Give the extent of all Plasmodium ovale-infected red blood cells.
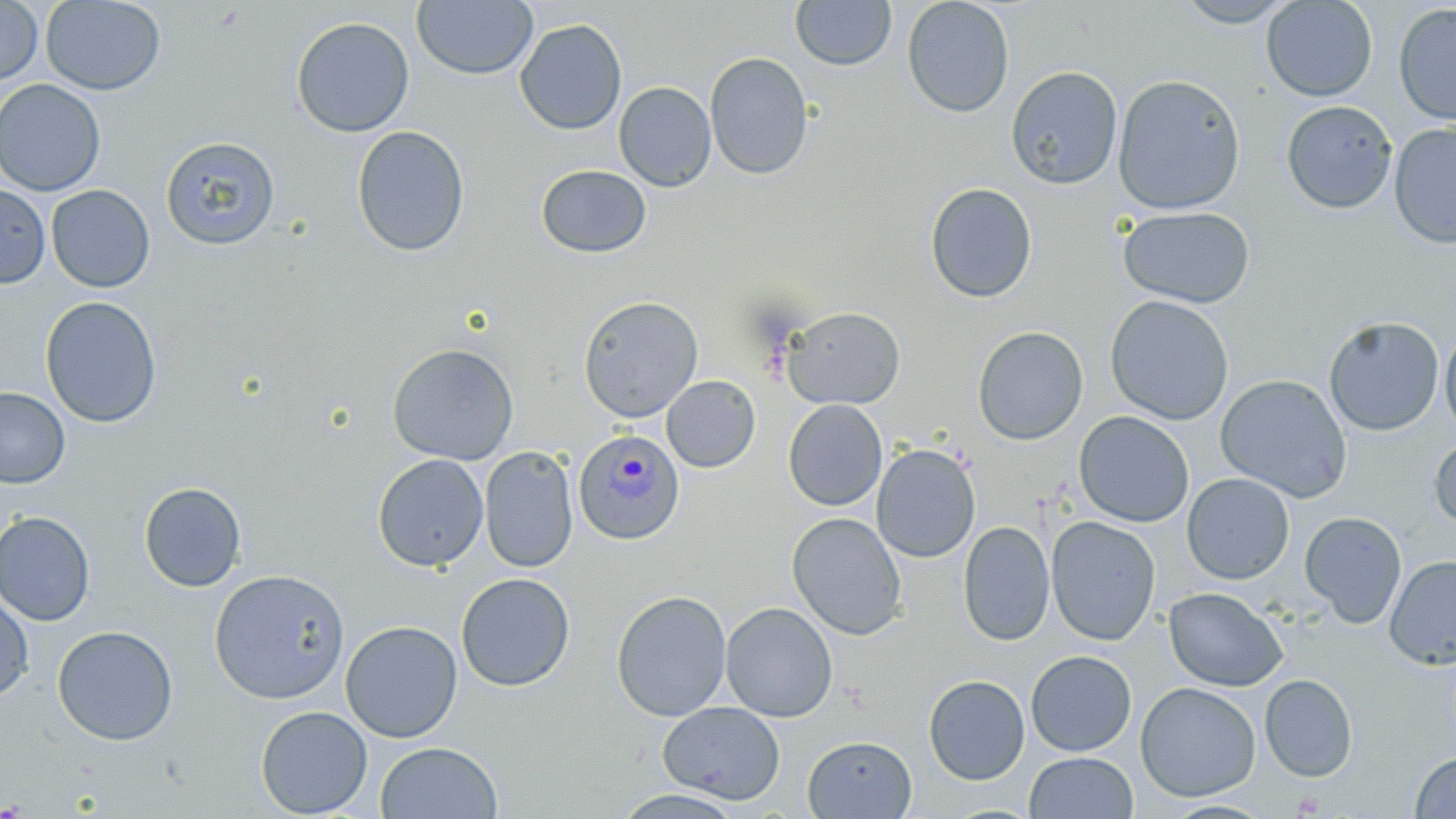
Approximate bounding boxes as (x1, y1, x2, y2) in pixels.
Plasmodium ovale-infected red blood cells: (573, 428, 686, 545).

Summary:
  - Uninfected red blood cell locations: (411, 0, 539, 81), (901, 0, 1015, 118), (1171, 0, 1300, 28), (1261, 0, 1378, 102), (0, 1, 43, 86), (40, 1, 166, 95), (790, 1, 896, 71), (1392, 3, 1456, 126), (290, 15, 415, 137), (514, 18, 628, 136), (704, 52, 814, 180), (1006, 66, 1123, 190), (1112, 73, 1247, 214), (0, 78, 106, 197), (613, 81, 717, 192), (1280, 100, 1398, 214), (1389, 121, 1456, 249), (351, 125, 470, 257), (161, 136, 280, 250), (535, 164, 653, 259), (923, 182, 1038, 303), (0, 183, 50, 289), (46, 185, 155, 293), (1116, 206, 1255, 308), (577, 295, 704, 422), (1104, 295, 1234, 425), (40, 296, 162, 428), (782, 306, 906, 410), (1323, 316, 1445, 436), (972, 325, 1088, 445), (1439, 328, 1456, 436), (386, 343, 520, 465), (1215, 374, 1352, 503), (661, 375, 761, 473), (0, 387, 71, 489), (782, 399, 888, 511), (1073, 411, 1195, 527), (1429, 433, 1456, 532), (871, 443, 981, 563), (479, 446, 579, 574), (372, 453, 489, 571), (1181, 473, 1295, 585), (138, 481, 247, 592), (0, 510, 96, 627), (1300, 511, 1407, 628), (786, 512, 908, 640), (1045, 515, 1161, 646), (957, 519, 1055, 646), (1384, 555, 1456, 669), (209, 568, 350, 704), (456, 572, 575, 692), (1164, 587, 1288, 691), (611, 589, 732, 721), (0, 592, 34, 703), (719, 601, 838, 722), (340, 620, 462, 743), (52, 625, 179, 746), (1025, 650, 1137, 756), (923, 674, 1030, 785), (1259, 674, 1358, 782), (1135, 682, 1262, 801), (657, 701, 785, 804), (255, 706, 373, 818), (802, 734, 917, 818), (375, 741, 503, 818), (1024, 751, 1138, 818), (1409, 751, 1456, 818), (1158, 800, 1277, 819)
  - Slide-level diagnosis: Plasmodium ovale
  - Field of view: one of a larger specimen
  - Image size: 1456×819 pixels
  - Modality: optical microscopy
  - Preparation: thin blood smear
  - Stain: May-Grünwald-Giemsa
  - Magnification: 1000x